Point out every malaria parasite and every leukocyte.
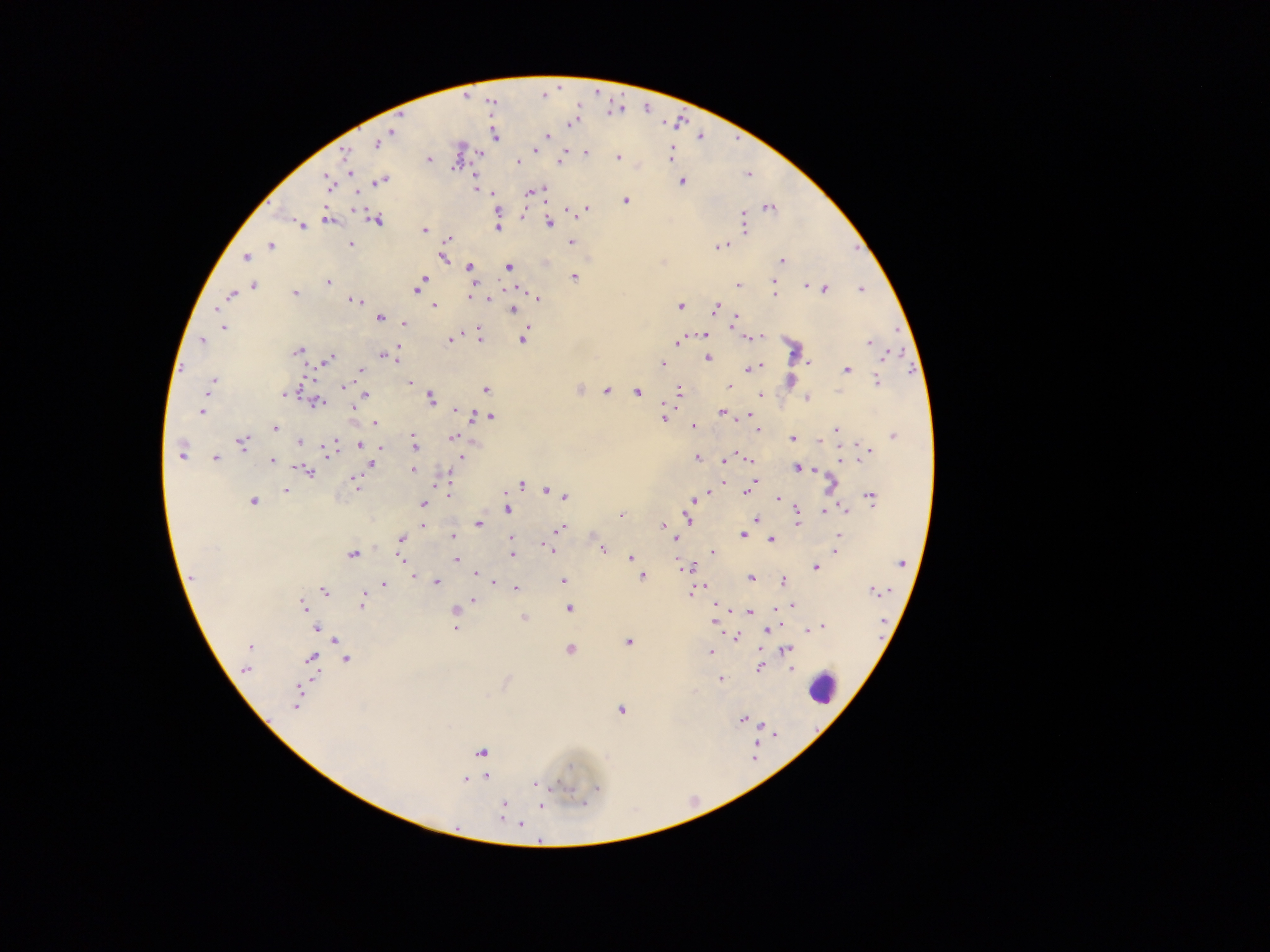

Approximate centers as {x, y} in pixels.
Malaria parasites: {571, 123}, {394, 131}, {494, 136}, {546, 136}, {377, 144}, {535, 150}, {586, 152}, {479, 153}, {345, 154}, {670, 154}, {617, 157}, {429, 160}, {518, 162}, {559, 162}, {350, 171}, {382, 180}, {327, 182}, {682, 182}, {542, 189}, {529, 192}, {626, 200}, {769, 208}, {586, 209}, {497, 212}, {376, 219}, {328, 220}, {548, 222}, {743, 224}, {302, 225}, {497, 228}, {425, 230}, {448, 238}, {572, 242}, {351, 244}, {270, 246}, {719, 246}, {442, 257}, {246, 258}, {781, 261}, {470, 267}, {508, 267}, {573, 277}, {423, 280}, {328, 282}, {474, 282}, {773, 283}, {420, 284}, {738, 285}, {806, 285}, {254, 286}, {417, 288}, {824, 289}, {861, 289}, {295, 293}, {775, 294}, {231, 295}, {470, 297}, {538, 298}, {488, 299}, {355, 301}, {680, 305}, {435, 307}, {715, 308}, {512, 309}, {736, 317}, {380, 318}, {404, 324}, {223, 328}, {479, 334}, {704, 335}, {756, 338}, {522, 339}, {450, 340}, {202, 341}, {676, 341}, {869, 342}, {398, 346}, {298, 350}, {887, 354}, {383, 355}, {395, 356}, {329, 358}, {708, 358}, {809, 362}, {662, 364}, {755, 367}, {361, 369}, {846, 369}, {214, 380}, {877, 380}, {410, 383}, {729, 386}, {344, 387}, {350, 389}, {486, 389}, {579, 389}, {210, 391}, {607, 391}, {679, 391}, {637, 392}, {365, 394}, {760, 395}, {283, 396}, {807, 398}, {430, 399}, {317, 402}, {354, 409}, {455, 410}, {201, 411}, {462, 412}, {722, 412}, {475, 415}, {750, 416}, {491, 417}, {664, 418}, {375, 422}, {693, 427}, {274, 428}, {758, 430}, {836, 430}, {893, 436}, {453, 437}, {792, 439}, {820, 441}, {299, 442}, {242, 443}, {360, 444}, {414, 445}, {330, 448}, {380, 448}, {868, 450}, {180, 454}, {461, 458}, {697, 458}, {216, 459}, {750, 459}, {841, 459}, {272, 460}, {726, 460}, {371, 463}, {796, 468}, {813, 469}, {413, 470}, {309, 471}, {355, 481}, {521, 485}, {831, 485}, {751, 487}, {546, 490}, {286, 491}, {747, 491}, {449, 494}, {707, 494}, {564, 496}, {778, 498}, {871, 498}, {693, 501}, {254, 502}, {423, 504}, {508, 509}, {797, 509}, {844, 510}, {825, 512}, {620, 515}, {688, 517}, {756, 520}, {797, 522}, {478, 524}, {423, 525}, {663, 525}, {560, 529}, {742, 535}, {839, 536}, {453, 537}, {512, 538}, {674, 538}, {400, 539}, {771, 541}, {548, 548}, {603, 548}, {836, 551}, {713, 552}, {352, 554}, {511, 555}, {630, 557}, {401, 559}, {456, 559}, {901, 563}, {683, 567}, {816, 568}, {477, 573}, {414, 576}, {191, 577}, {641, 577}, {751, 578}, {564, 580}, {784, 581}, {495, 582}, {437, 583}, {384, 585}, {515, 588}, {874, 590}, {323, 591}, {691, 592}, {474, 600}, {363, 602}, {303, 605}, {718, 605}, {791, 605}, {455, 608}, {569, 609}, {749, 611}, {523, 617}, {713, 622}, {821, 627}, {317, 628}, {454, 628}, {810, 629}, {767, 630}, {736, 637}, {628, 642}, {249, 646}, {569, 650}, {787, 650}, {710, 651}, {311, 658}, {347, 659}, {758, 668}, {791, 668}, {246, 669}, {722, 680}, {296, 700}, {621, 711}, {743, 719}, {481, 753}, {569, 768}, {487, 777}, {465, 780}, {536, 783}, {598, 788}, {582, 802}, {504, 804}, {541, 806}, {520, 824}.
Leukocytes: {822, 690}.

Thick blood film. Image is 1270×952 pixels. Mobile-phone photograph taken through the microscope. Collected in Ghana. One field of view.